Point out each Plasmodium parasite.
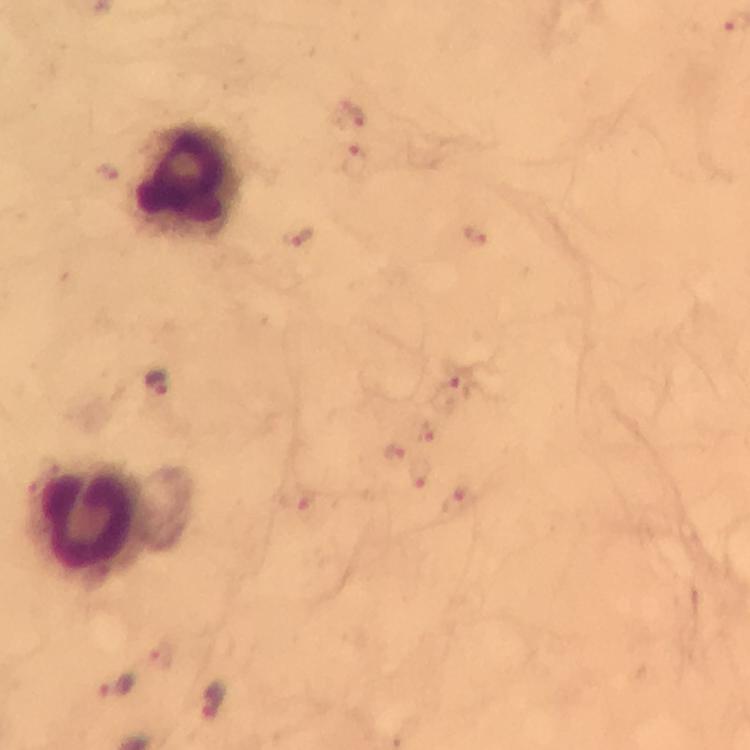
Approximate centers as (x, y) in pixels.
Plasmodium parasites: (350, 114), (357, 162), (297, 236), (158, 380), (450, 388), (393, 452), (116, 686), (216, 703).

capture: smartphone mounted on the microscope
context: from a diagnostic examination for malaria
cropped_from: one field of view
immersion_oil: applied
preparation: thick blood film
image_size: 750×750 pixels
stain: Giemsa
magnification: 100x
leukocyte_locations: 'approximate centers as (x, y) in pixels: (186, 180), (90, 522)'